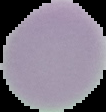

Summary:
  - Result: no malaria parasites detected
  - Preparation: thin blood film
  - Image type: cell region segmented out of the field of view; surrounding area masked to black
  - Image size: 106×112 pixels